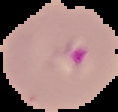
Result: malaria parasites detected. Image is 118×112 pixels. From a thin blood film. The area outside the segmented cell region is set to black.